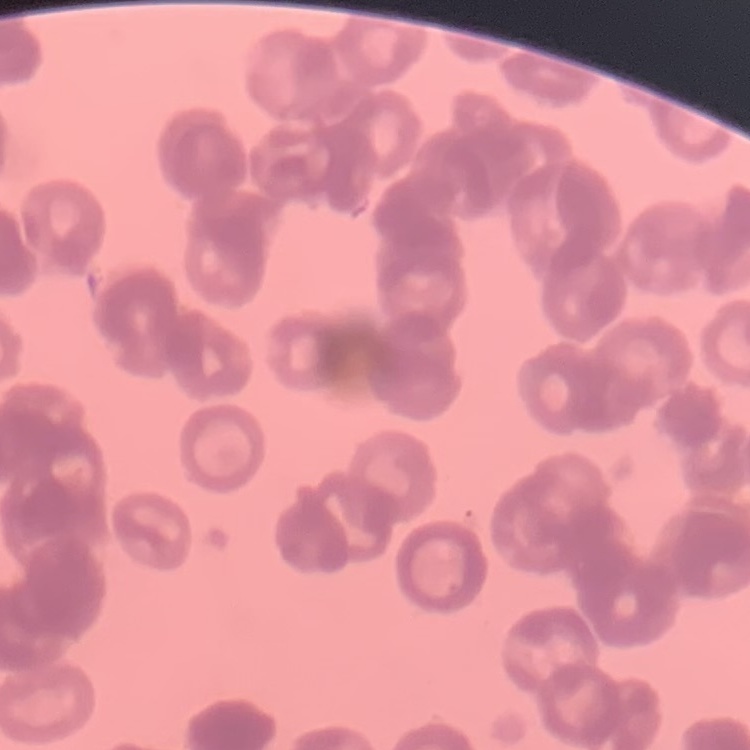
The erythrocytes exhibit rouleaux formation. Field's or Giemsa stain. One tile cut from a larger photomicrograph. Thin peripheral smear.